Assess this cell for malaria.
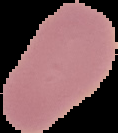

Uninfected.

From a thin blood film. Image is 118×133 pixels. Segmented cell region on a black background.